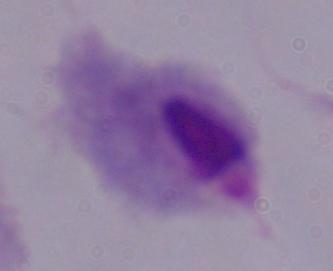
{
  "magnification": "1000x",
  "modality": "micrograph",
  "identification": "trichomonad"
}